State which parasite is depicted.
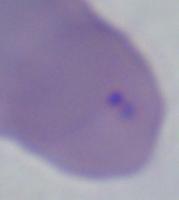
Babesia.

1000x magnification. Micrograph.